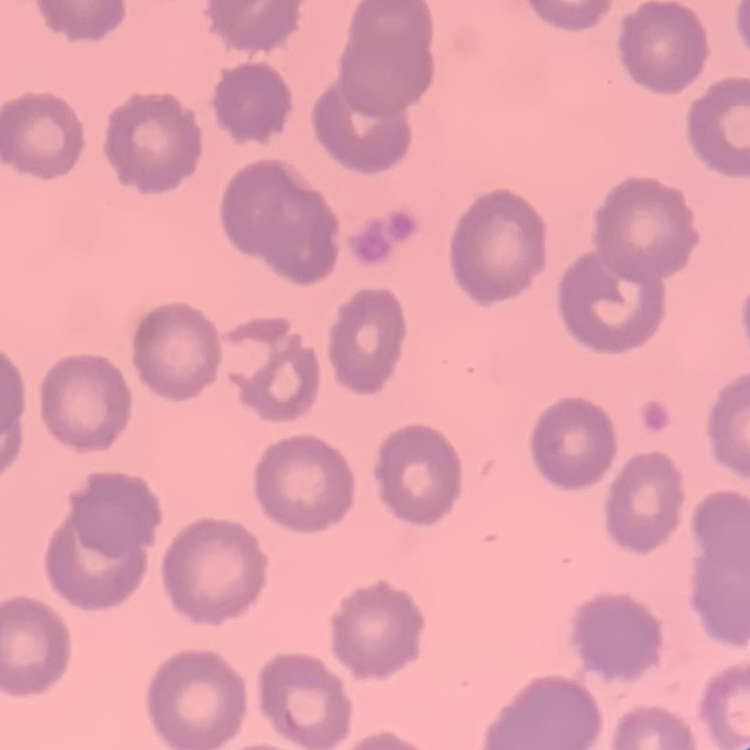
Summary:
  - Erythrocyte morphology: no rouleaux formation
  - Image type: one tile cut from a larger photomicrograph
  - Stain: Field's or Giemsa
  - Preparation: thin peripheral smear